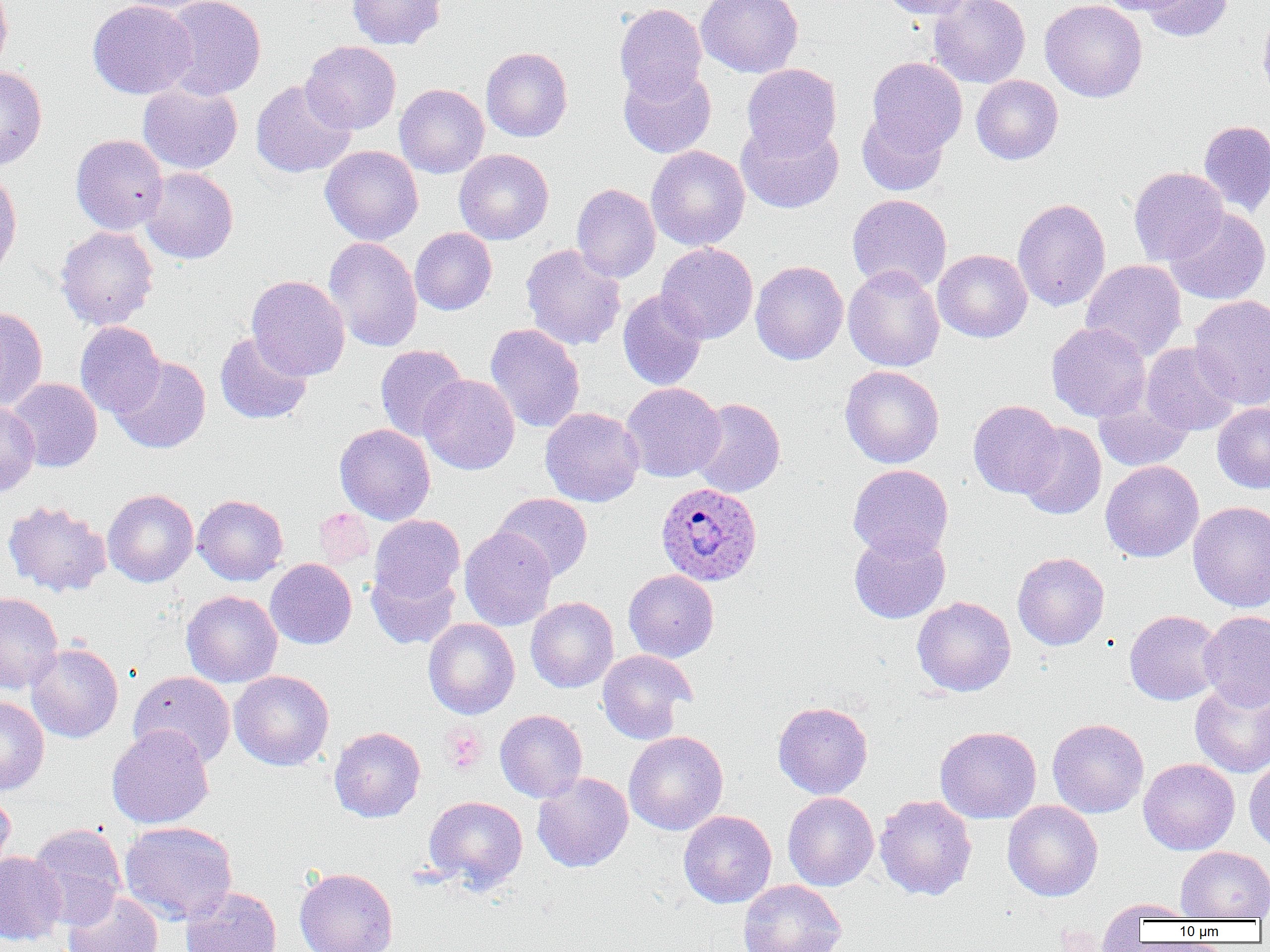
slide-level diagnosis = Plasmodium ovale
image size = 1270×952 pixels
preparation = thin blood film
modality = light microscopy
Plasmodium ovale-infected red blood cell locations = approximate bounding boxes as [x1, y1, x2, y2] in pixels: [655, 482, 762, 587]
platelet locations = approximate bounding boxes as [x1, y1, x2, y2] in pixels: [441, 725, 487, 775]
field of view = single
uninfected red blood cell locations = approximate bounding boxes as [x1, y1, x2, y2] in pixels: [0, 0, 12, 76], [87, 0, 198, 99], [114, 0, 223, 14], [160, 0, 266, 100], [347, 0, 446, 49], [696, 0, 804, 78], [878, 0, 975, 19], [928, 0, 1030, 88], [1039, 0, 1148, 103], [1096, 0, 1192, 16], [1139, 0, 1234, 42], [614, 3, 707, 103], [1258, 8, 1270, 108], [301, 41, 401, 135], [481, 46, 573, 142], [866, 56, 967, 157], [742, 63, 841, 158], [0, 66, 47, 171], [618, 66, 716, 158], [971, 75, 1063, 165], [250, 79, 356, 178], [138, 83, 242, 175], [394, 83, 489, 178], [857, 107, 950, 196], [736, 119, 844, 214], [1198, 119, 1270, 217], [70, 134, 169, 235], [321, 145, 423, 245], [646, 146, 750, 251], [454, 149, 553, 244], [140, 167, 238, 264], [1128, 167, 1228, 266], [0, 168, 22, 279], [571, 183, 660, 284], [847, 194, 952, 294], [1012, 198, 1111, 312], [1165, 206, 1269, 305], [55, 225, 159, 329], [410, 227, 497, 315], [323, 236, 423, 353], [656, 242, 758, 344], [520, 244, 626, 350], [933, 249, 1032, 342], [750, 260, 849, 365], [1081, 260, 1186, 361], [843, 265, 945, 372], [246, 275, 350, 380], [617, 289, 708, 391], [1189, 294, 1270, 410], [0, 305, 48, 412], [75, 321, 166, 418], [1046, 321, 1150, 422], [485, 323, 585, 433], [215, 331, 313, 425], [1141, 342, 1241, 436], [375, 345, 469, 441], [110, 356, 211, 454], [839, 365, 944, 468], [420, 374, 520, 475], [7, 378, 102, 472], [621, 382, 725, 482], [1093, 391, 1194, 472], [688, 397, 786, 498], [968, 400, 1063, 498], [0, 402, 40, 497], [1212, 403, 1270, 493], [540, 407, 644, 507], [1016, 422, 1107, 520], [335, 423, 435, 525], [1100, 460, 1204, 563], [847, 464, 953, 560], [103, 489, 198, 587], [492, 493, 593, 582], [192, 494, 288, 586], [2, 499, 112, 598], [1188, 501, 1270, 612], [313, 508, 375, 569], [369, 514, 465, 606], [459, 526, 557, 631], [849, 528, 950, 624], [1012, 552, 1110, 650], [265, 558, 356, 649], [367, 564, 460, 649], [623, 569, 719, 662], [181, 590, 282, 687], [0, 592, 63, 694], [526, 596, 618, 693], [913, 596, 1016, 696], [1124, 610, 1224, 705], [1198, 611, 1270, 711], [423, 618, 520, 719], [26, 643, 124, 743], [597, 650, 696, 743], [229, 670, 334, 771], [128, 671, 236, 768], [1189, 679, 1270, 778], [0, 695, 49, 795], [773, 701, 873, 799], [495, 709, 587, 802], [1047, 718, 1149, 818], [107, 725, 214, 829], [934, 725, 1042, 823], [329, 726, 426, 822], [623, 730, 728, 836], [1244, 757, 1270, 853], [1138, 758, 1240, 855], [532, 772, 633, 873], [0, 790, 16, 882], [782, 792, 879, 890], [874, 794, 977, 901], [423, 795, 528, 892], [1003, 800, 1103, 901], [678, 810, 776, 908], [119, 820, 238, 925], [27, 822, 127, 929], [1176, 846, 1270, 921], [0, 851, 66, 946], [294, 867, 398, 952], [738, 879, 847, 952], [180, 887, 282, 952], [64, 892, 164, 952], [1100, 899, 1200, 926]
magnification = 1000x